Assess the morphology of the red blood cells.
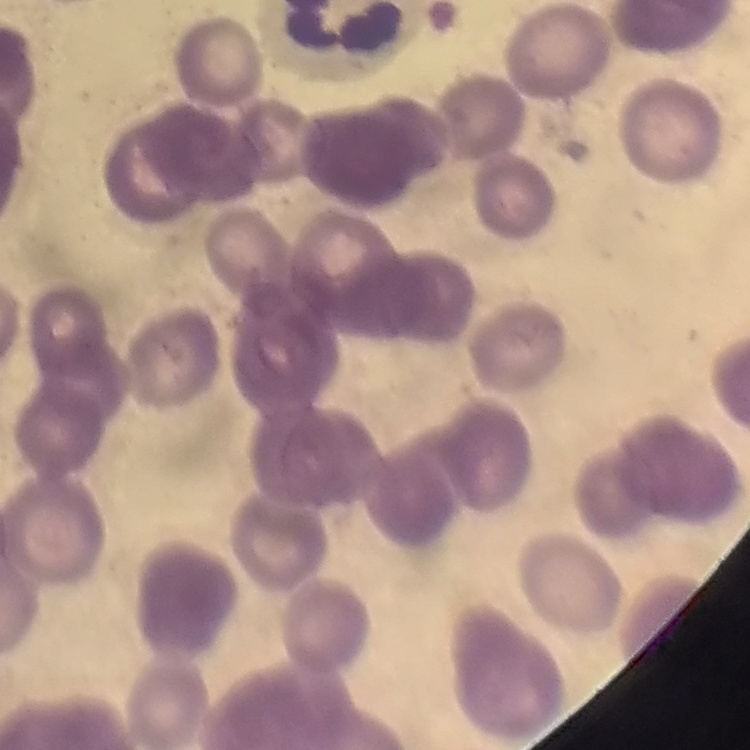

They show rouleaux formation.

{
  "preparation": "thin blood film",
  "image_type": "one tile cut from a larger photomicrograph",
  "stain": "Field's or Giemsa"
}